State which parasite is depicted.
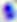

Toxoplasma gondii.

magnification = 400x
modality = micrograph